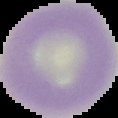
preparation = thin blood smear
image size = 118×118 pixels
image type = segmented cell region on a black background
result = no Plasmodium parasites detected